Locate every Plasmodium parasite.
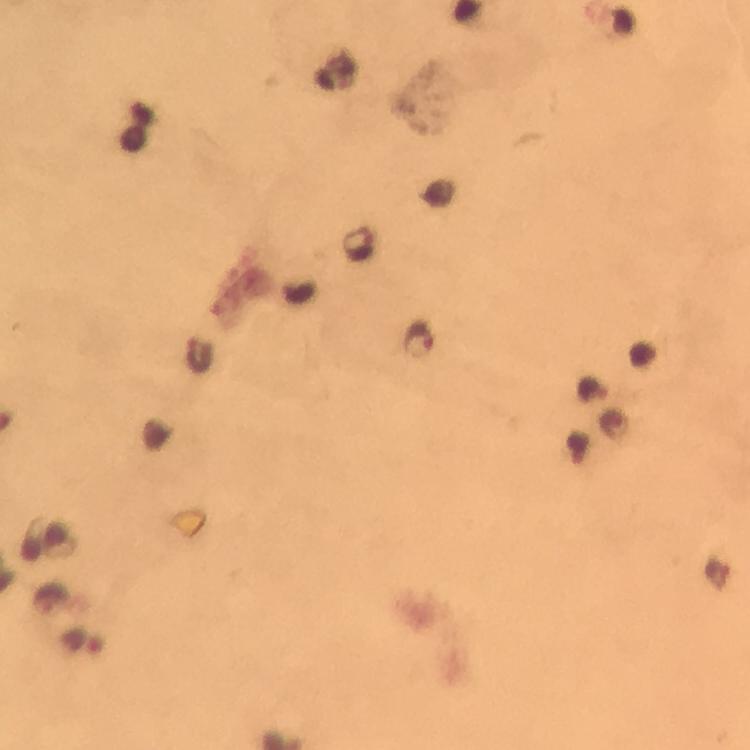
Approximate centers as (x, y) in pixels.
Plasmodium parasites: (359, 244), (418, 339), (594, 389), (82, 641).

Image is 750×750 pixels. 100x magnification. A crop from one field of view. Giemsa stain. From a diagnostic examination for malaria. Thick blood smear. Photographed with a smartphone mounted on the microscope. Immersion oil applied.